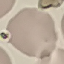
Summary:
  - Result: no malaria parasites detected
  - Stain: Giemsa
  - Preparation: thin smear
  - Image type: cell patch, automatically extracted from a larger field of view and resized to 64 × 64 pixels
  - Capture: smartphone through the microscope eyepiece